Give the position of every malaria parasite.
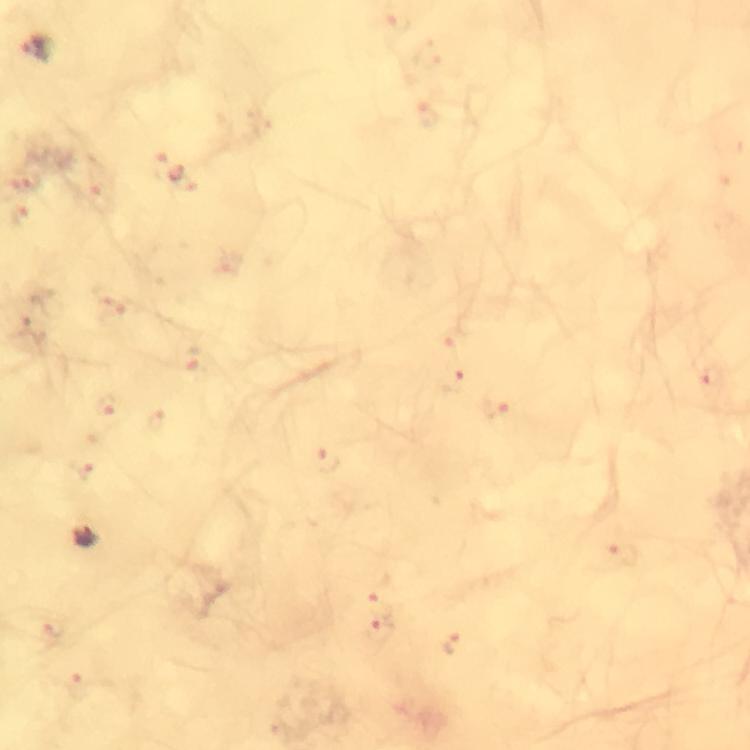
Approximate centers as [x, y] in pixels.
Malaria parasites: [37, 46], [711, 378], [451, 382], [495, 408], [326, 462], [83, 538], [623, 555], [376, 607], [380, 632], [452, 644].

At 100x magnification. A crop from one field of view. Immersion oil was used. From a diagnostic examination for malaria. Smartphone photograph taken through a microscope. Giemsa-stained preparation. Image is 750×750 pixels. Thick smear.